Classify this cell by malaria status.
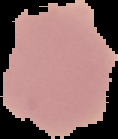

Uninfected.

Summary:
  - Image type: segmented cell region on a black background
  - Image size: 118×139 pixels
  - Preparation: thin blood smear